Give a bounding box for every leukocyte visible.
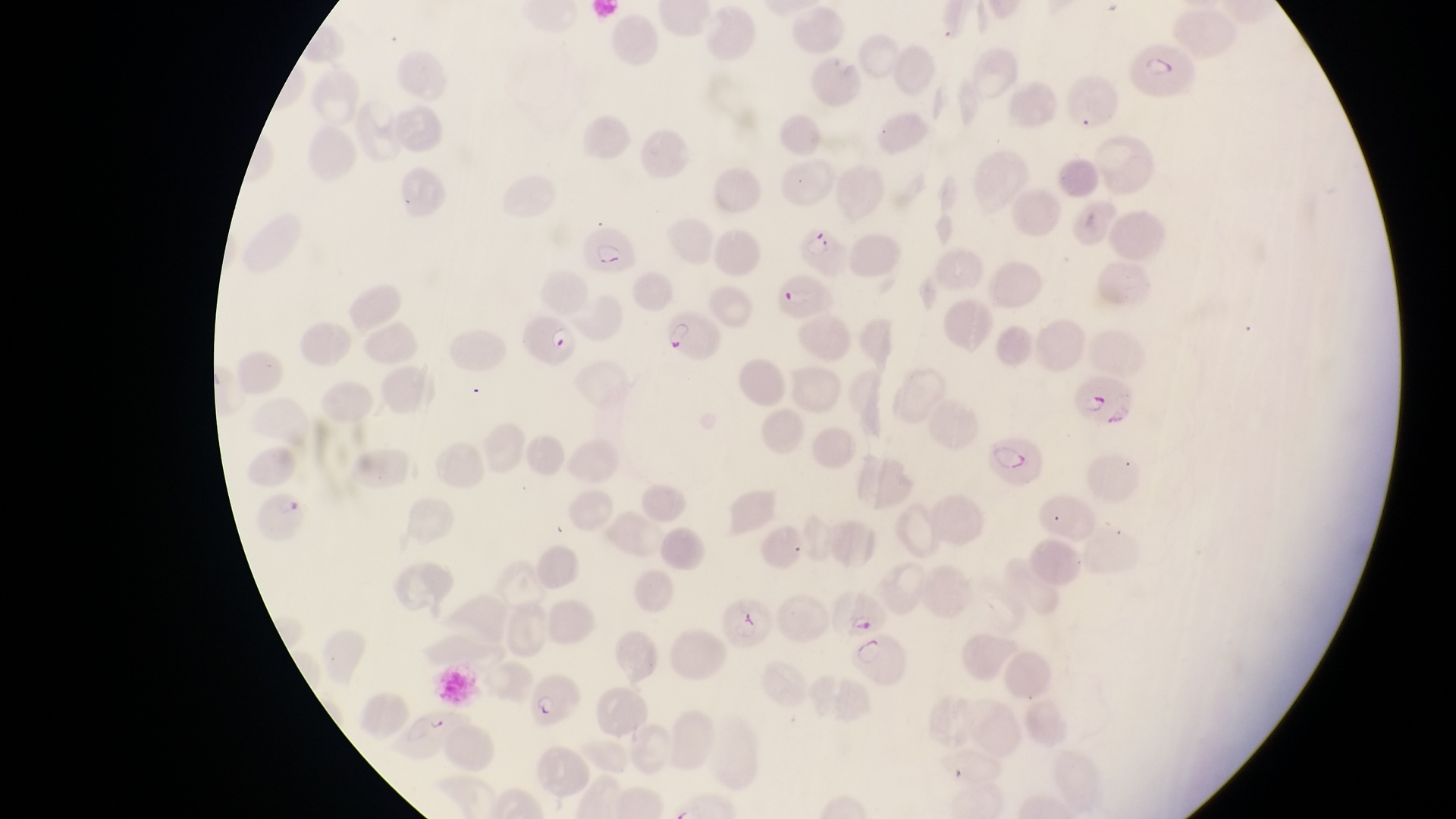

No leukocytes observed.

Approximate bounding boxes as [left, top, right, bottom] in pixels. Parasitised red blood cell locations: [1125, 39, 1199, 97], [795, 214, 848, 273], [584, 235, 637, 277], [772, 270, 835, 323], [519, 307, 575, 368], [661, 314, 720, 363], [1073, 376, 1134, 428], [986, 433, 1046, 489], [245, 494, 312, 543], [838, 588, 888, 635], [719, 602, 769, 651], [848, 634, 914, 692], [528, 664, 581, 724]. Artifact (platelet-like body, stain precipitate, or debris) locations: [422, 716, 455, 740]. Image is 1456×819 pixels. Magnification of 1000x. Sample from Uganda. Thin blood film. Captured by a smartphone held over the eyepiece of an Olympus CX-23 microscope. One field of view.